Give the extent of all Plasmodium vivax-infected red blood cells.
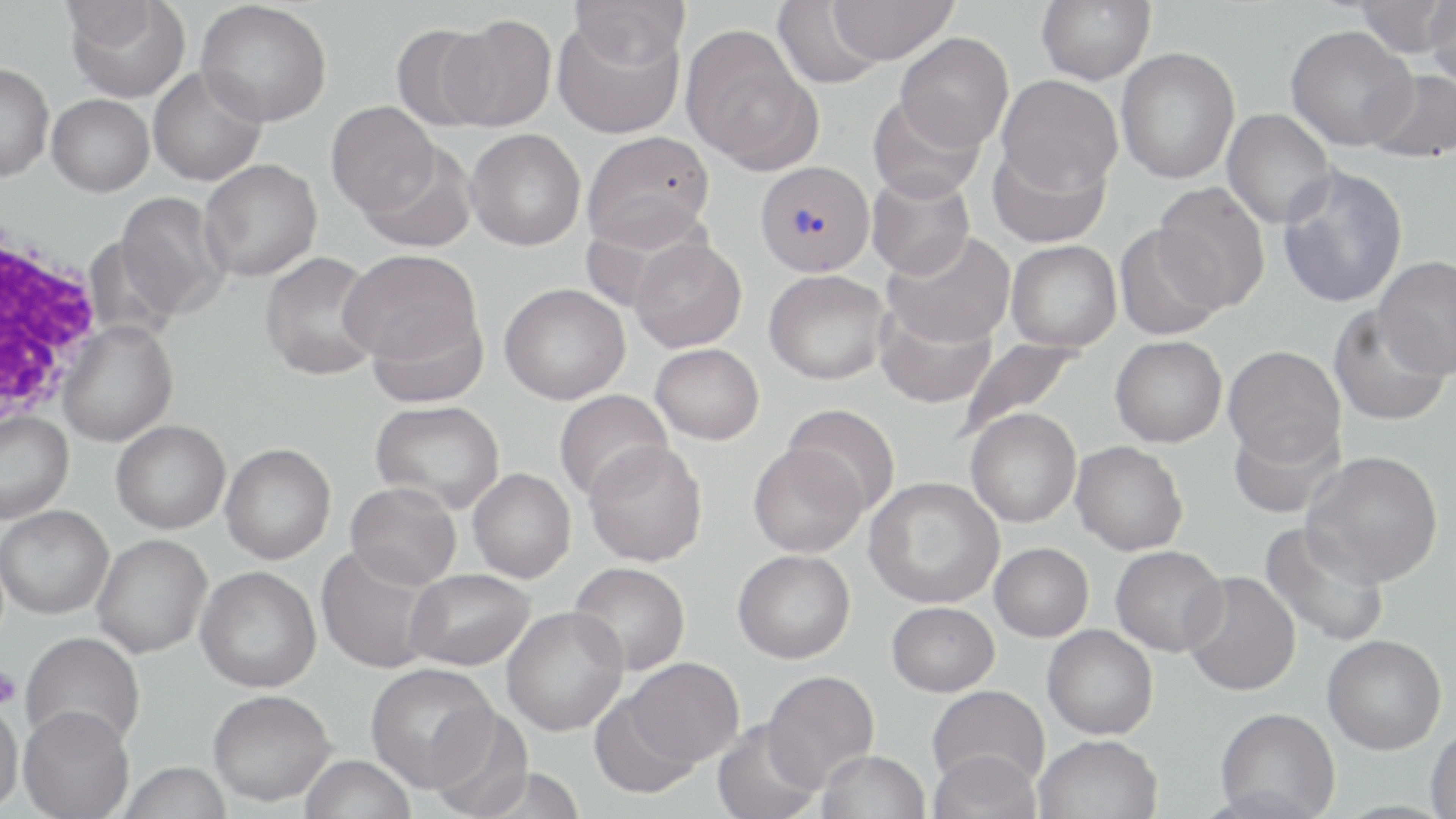
Approximate bounding boxes as named x1/y1/x2/y2 corners in pixels.
Plasmodium vivax-infected red blood cells: (x1=753, y1=161, x2=875, y2=277).

Summary:
  - Uninfected red blood cell locations: (x1=64, y1=0, x2=190, y2=102), (x1=570, y1=0, x2=691, y2=68), (x1=825, y1=0, x2=957, y2=64), (x1=1036, y1=0, x2=1156, y2=86), (x1=1353, y1=0, x2=1455, y2=58), (x1=1423, y1=0, x2=1456, y2=89), (x1=196, y1=1, x2=331, y2=127), (x1=772, y1=1, x2=888, y2=89), (x1=552, y1=14, x2=685, y2=138), (x1=441, y1=15, x2=557, y2=131), (x1=390, y1=24, x2=494, y2=131), (x1=680, y1=25, x2=821, y2=173), (x1=1285, y1=25, x2=1416, y2=151), (x1=895, y1=32, x2=1014, y2=151), (x1=1116, y1=47, x2=1240, y2=184), (x1=0, y1=63, x2=54, y2=181), (x1=148, y1=66, x2=267, y2=186), (x1=1365, y1=69, x2=1456, y2=163), (x1=997, y1=75, x2=1122, y2=194), (x1=47, y1=94, x2=154, y2=197), (x1=868, y1=94, x2=985, y2=203), (x1=326, y1=101, x2=439, y2=216), (x1=1222, y1=109, x2=1336, y2=229), (x1=466, y1=128, x2=586, y2=250), (x1=581, y1=131, x2=715, y2=250), (x1=988, y1=139, x2=1111, y2=248), (x1=359, y1=143, x2=477, y2=253), (x1=199, y1=159, x2=322, y2=282), (x1=1278, y1=165, x2=1408, y2=308), (x1=866, y1=171, x2=975, y2=280), (x1=1152, y1=183, x2=1270, y2=312), (x1=115, y1=191, x2=231, y2=320), (x1=1114, y1=225, x2=1227, y2=340), (x1=882, y1=231, x2=1015, y2=348), (x1=629, y1=237, x2=747, y2=352), (x1=1005, y1=240, x2=1122, y2=352), (x1=340, y1=249, x2=483, y2=371), (x1=260, y1=252, x2=383, y2=381), (x1=1374, y1=256, x2=1456, y2=380), (x1=764, y1=270, x2=890, y2=384), (x1=499, y1=283, x2=630, y2=404), (x1=874, y1=300, x2=996, y2=409), (x1=367, y1=301, x2=489, y2=408), (x1=1328, y1=304, x2=1450, y2=427), (x1=58, y1=321, x2=178, y2=447), (x1=1110, y1=335, x2=1227, y2=447), (x1=956, y1=337, x2=1086, y2=442), (x1=650, y1=343, x2=764, y2=444), (x1=1223, y1=345, x2=1346, y2=467), (x1=554, y1=389, x2=672, y2=502), (x1=370, y1=400, x2=505, y2=513), (x1=782, y1=403, x2=901, y2=515), (x1=965, y1=408, x2=1081, y2=528), (x1=0, y1=411, x2=74, y2=523), (x1=1229, y1=417, x2=1343, y2=520), (x1=111, y1=420, x2=231, y2=534), (x1=583, y1=440, x2=708, y2=566), (x1=1071, y1=441, x2=1188, y2=556), (x1=220, y1=443, x2=336, y2=564), (x1=748, y1=443, x2=866, y2=557), (x1=1302, y1=451, x2=1443, y2=587), (x1=468, y1=468, x2=576, y2=583), (x1=865, y1=477, x2=1004, y2=609), (x1=345, y1=482, x2=461, y2=589), (x1=1, y1=505, x2=113, y2=618), (x1=1260, y1=521, x2=1392, y2=649), (x1=91, y1=533, x2=212, y2=659), (x1=990, y1=542, x2=1093, y2=641), (x1=316, y1=545, x2=443, y2=674), (x1=1111, y1=545, x2=1227, y2=657), (x1=733, y1=549, x2=855, y2=663), (x1=569, y1=562, x2=690, y2=675), (x1=195, y1=565, x2=321, y2=693), (x1=405, y1=569, x2=535, y2=670), (x1=1181, y1=571, x2=1301, y2=697), (x1=886, y1=601, x2=999, y2=697), (x1=502, y1=606, x2=629, y2=735), (x1=1043, y1=624, x2=1158, y2=739), (x1=21, y1=631, x2=145, y2=750), (x1=1322, y1=634, x2=1446, y2=754), (x1=625, y1=657, x2=743, y2=767), (x1=365, y1=663, x2=496, y2=791), (x1=762, y1=670, x2=879, y2=788), (x1=927, y1=685, x2=1050, y2=790), (x1=208, y1=689, x2=336, y2=805), (x1=589, y1=690, x2=703, y2=800), (x1=0, y1=695, x2=24, y2=815), (x1=18, y1=704, x2=135, y2=819), (x1=426, y1=706, x2=534, y2=818), (x1=1215, y1=707, x2=1340, y2=819), (x1=712, y1=719, x2=824, y2=819), (x1=1426, y1=726, x2=1456, y2=818), (x1=1034, y1=734, x2=1162, y2=819), (x1=927, y1=749, x2=1043, y2=817), (x1=817, y1=750, x2=931, y2=819), (x1=299, y1=755, x2=416, y2=819), (x1=118, y1=761, x2=233, y2=819)
  - Platelet locations: (x1=0, y1=667, x2=21, y2=708)
  - White blood cell locations: (x1=0, y1=221, x2=106, y2=433)
  - Slide-level diagnosis: Plasmodium vivax
  - Preparation: thin blood smear
  - Magnification: 1000x
  - Image size: 1456×819 pixels
  - Stain: May-Grünwald-Giemsa
  - Field of view: one of a larger specimen
  - Modality: light microscopy